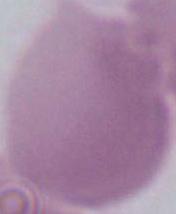

{
  "magnification": "1000x",
  "modality": "micrograph",
  "identification": "red blood cell"
}